Assess the morphology of the erythrocytes.
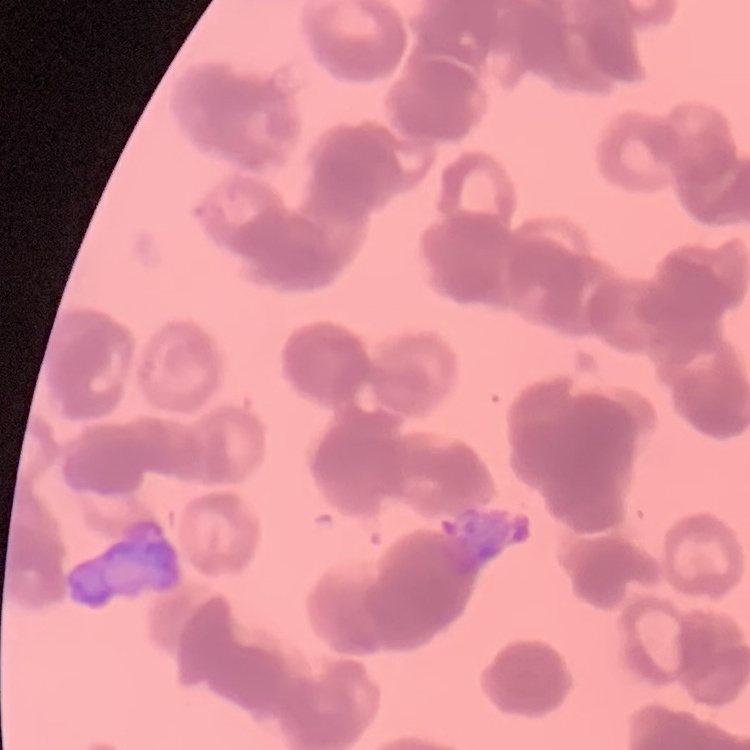

They show rouleaux formation.

preparation = thin peripheral smear
stain = Field's or Giemsa
image type = one tile cut from a larger photomicrograph